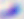

modality = photomicrograph
magnification = 400x
identification = Toxoplasma gondii